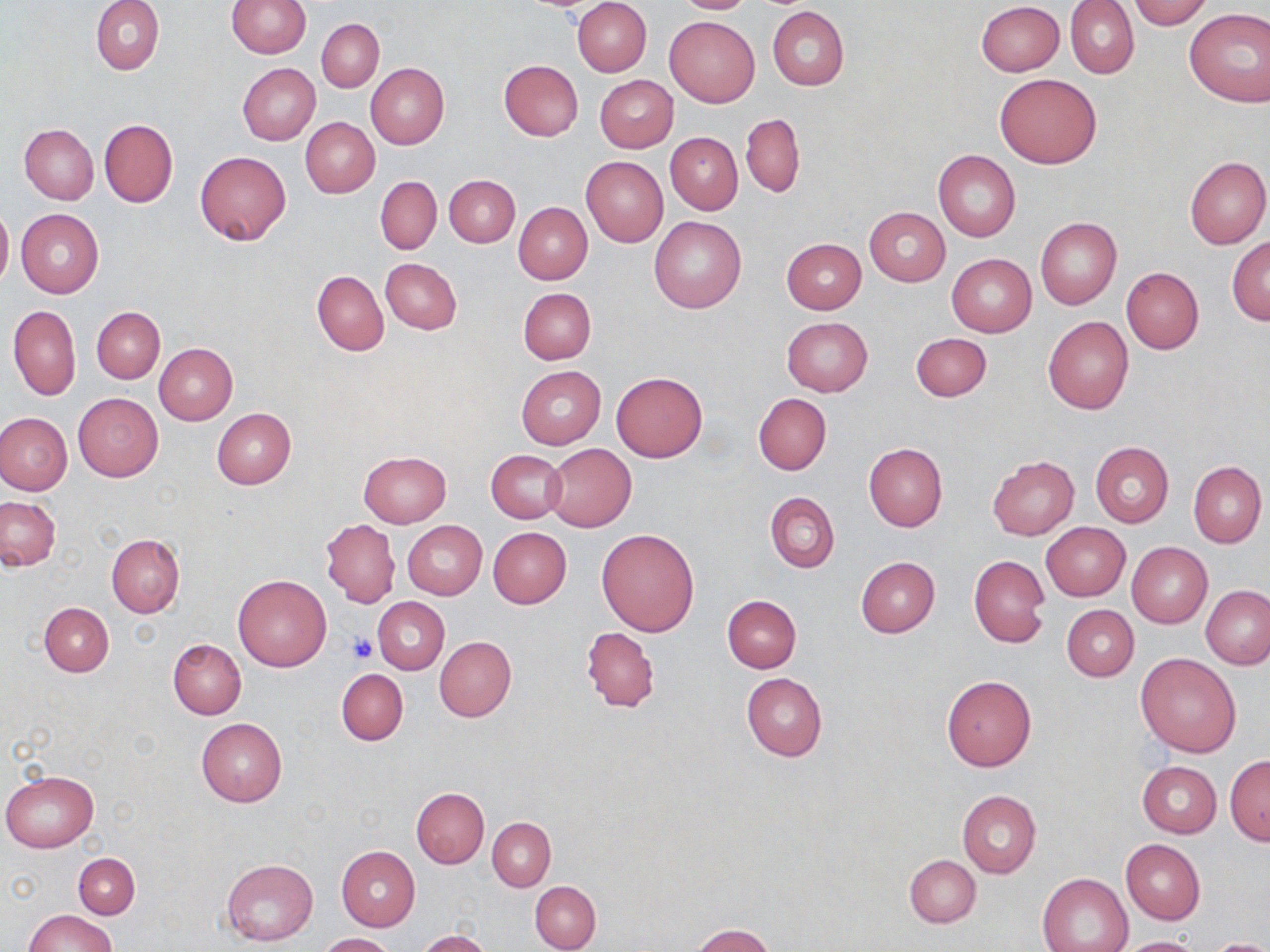

{
  "slide_level_diagnosis": "no evidence of blood parasites",
  "platelet_locations": "approximate bounding boxes as named x1/y1/x2/y2 corners in pixels: (x1=347, y1=632, x2=377, y2=663)",
  "uninfected_red_blood_cell_locations": "approximate bounding boxes as named x1/y1/x2/y2 corners in pixels: (x1=92, y1=0, x2=164, y2=74), (x1=226, y1=0, x2=310, y2=58), (x1=573, y1=0, x2=652, y2=76), (x1=674, y1=0, x2=758, y2=14), (x1=1128, y1=0, x2=1212, y2=30), (x1=976, y1=1, x2=1064, y2=76), (x1=1067, y1=1, x2=1140, y2=79), (x1=767, y1=6, x2=849, y2=90), (x1=1184, y1=7, x2=1270, y2=107), (x1=664, y1=16, x2=759, y2=106), (x1=317, y1=18, x2=384, y2=92), (x1=500, y1=60, x2=583, y2=141), (x1=365, y1=62, x2=449, y2=149), (x1=237, y1=63, x2=321, y2=145), (x1=994, y1=73, x2=1102, y2=168), (x1=595, y1=75, x2=678, y2=152), (x1=740, y1=114, x2=804, y2=198), (x1=300, y1=117, x2=380, y2=198), (x1=99, y1=118, x2=178, y2=207), (x1=20, y1=123, x2=98, y2=204), (x1=665, y1=132, x2=742, y2=214), (x1=933, y1=149, x2=1020, y2=242), (x1=194, y1=150, x2=291, y2=246), (x1=581, y1=155, x2=668, y2=247), (x1=1185, y1=156, x2=1270, y2=248), (x1=445, y1=175, x2=519, y2=247), (x1=376, y1=176, x2=442, y2=254), (x1=513, y1=203, x2=591, y2=284), (x1=0, y1=205, x2=12, y2=289), (x1=865, y1=207, x2=950, y2=286), (x1=16, y1=209, x2=104, y2=297), (x1=650, y1=217, x2=745, y2=313), (x1=1035, y1=217, x2=1121, y2=310), (x1=1227, y1=237, x2=1270, y2=324), (x1=781, y1=238, x2=866, y2=314), (x1=946, y1=253, x2=1037, y2=337), (x1=380, y1=258, x2=462, y2=334), (x1=1121, y1=268, x2=1204, y2=354), (x1=312, y1=271, x2=388, y2=355), (x1=517, y1=287, x2=597, y2=364), (x1=7, y1=305, x2=81, y2=400), (x1=92, y1=307, x2=165, y2=382), (x1=782, y1=317, x2=873, y2=397), (x1=1043, y1=317, x2=1133, y2=415), (x1=911, y1=333, x2=991, y2=402), (x1=153, y1=343, x2=237, y2=425), (x1=516, y1=366, x2=604, y2=449), (x1=611, y1=372, x2=707, y2=462), (x1=73, y1=393, x2=163, y2=482), (x1=753, y1=393, x2=831, y2=475), (x1=212, y1=408, x2=296, y2=489), (x1=0, y1=412, x2=73, y2=495), (x1=1090, y1=441, x2=1173, y2=528), (x1=863, y1=442, x2=948, y2=531), (x1=545, y1=444, x2=636, y2=532), (x1=486, y1=450, x2=566, y2=524), (x1=358, y1=451, x2=452, y2=527), (x1=987, y1=455, x2=1079, y2=540), (x1=1188, y1=461, x2=1266, y2=547), (x1=765, y1=492, x2=839, y2=573), (x1=1, y1=497, x2=60, y2=570), (x1=321, y1=518, x2=400, y2=607), (x1=402, y1=521, x2=487, y2=600), (x1=1041, y1=522, x2=1130, y2=601), (x1=488, y1=527, x2=572, y2=608), (x1=596, y1=528, x2=700, y2=636), (x1=106, y1=534, x2=185, y2=617), (x1=1127, y1=542, x2=1212, y2=628), (x1=969, y1=555, x2=1050, y2=648), (x1=855, y1=556, x2=940, y2=638), (x1=233, y1=574, x2=331, y2=671), (x1=1201, y1=585, x2=1270, y2=670), (x1=722, y1=594, x2=801, y2=672), (x1=373, y1=597, x2=449, y2=674), (x1=40, y1=603, x2=113, y2=677), (x1=1060, y1=604, x2=1139, y2=681), (x1=582, y1=626, x2=660, y2=713), (x1=434, y1=636, x2=517, y2=721), (x1=169, y1=639, x2=246, y2=719), (x1=1135, y1=653, x2=1241, y2=756), (x1=336, y1=668, x2=408, y2=745), (x1=741, y1=672, x2=827, y2=762), (x1=941, y1=675, x2=1036, y2=771), (x1=196, y1=718, x2=287, y2=806), (x1=1224, y1=755, x2=1270, y2=844), (x1=1138, y1=761, x2=1220, y2=837), (x1=1, y1=771, x2=97, y2=852), (x1=411, y1=787, x2=488, y2=867), (x1=956, y1=790, x2=1040, y2=879), (x1=487, y1=816, x2=555, y2=891), (x1=1121, y1=839, x2=1205, y2=924), (x1=336, y1=846, x2=420, y2=930), (x1=73, y1=853, x2=139, y2=918), (x1=905, y1=855, x2=980, y2=928), (x1=221, y1=858, x2=319, y2=945), (x1=1038, y1=873, x2=1133, y2=952), (x1=530, y1=881, x2=601, y2=951), (x1=24, y1=910, x2=117, y2=952), (x1=690, y1=925, x2=775, y2=952), (x1=417, y1=930, x2=491, y2=952), (x1=319, y1=933, x2=397, y2=952), (x1=1118, y1=936, x2=1205, y2=952), (x1=1206, y1=938, x2=1270, y2=952)",
  "modality": "optical microscopy",
  "preparation": "thin blood film",
  "field_of_view": "single",
  "stain": "May-Grünwald-Giemsa",
  "magnification": "1000x",
  "image_size": "1270×952 pixels"
}